Report the malaria status of this cell.
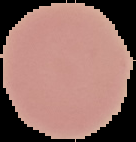

Uninfected.

Summary:
  - Image size: 136×142 pixels
  - Preparation: thin blood smear
  - Image type: segmented cell region on a black background